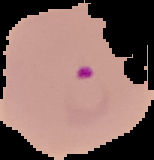
Summary:
  - Preparation: thin blood smear
  - Result: Plasmodium parasites identified
  - Image type: segmented cell region with the area outside set to black
  - Image size: 154×160 pixels